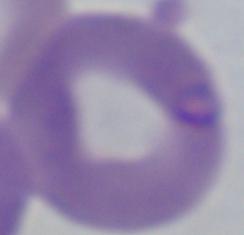

Photomicrograph. Captured at 1000x magnification. A Babesia parasite is seen.